Outline each blood parasite and name the species.
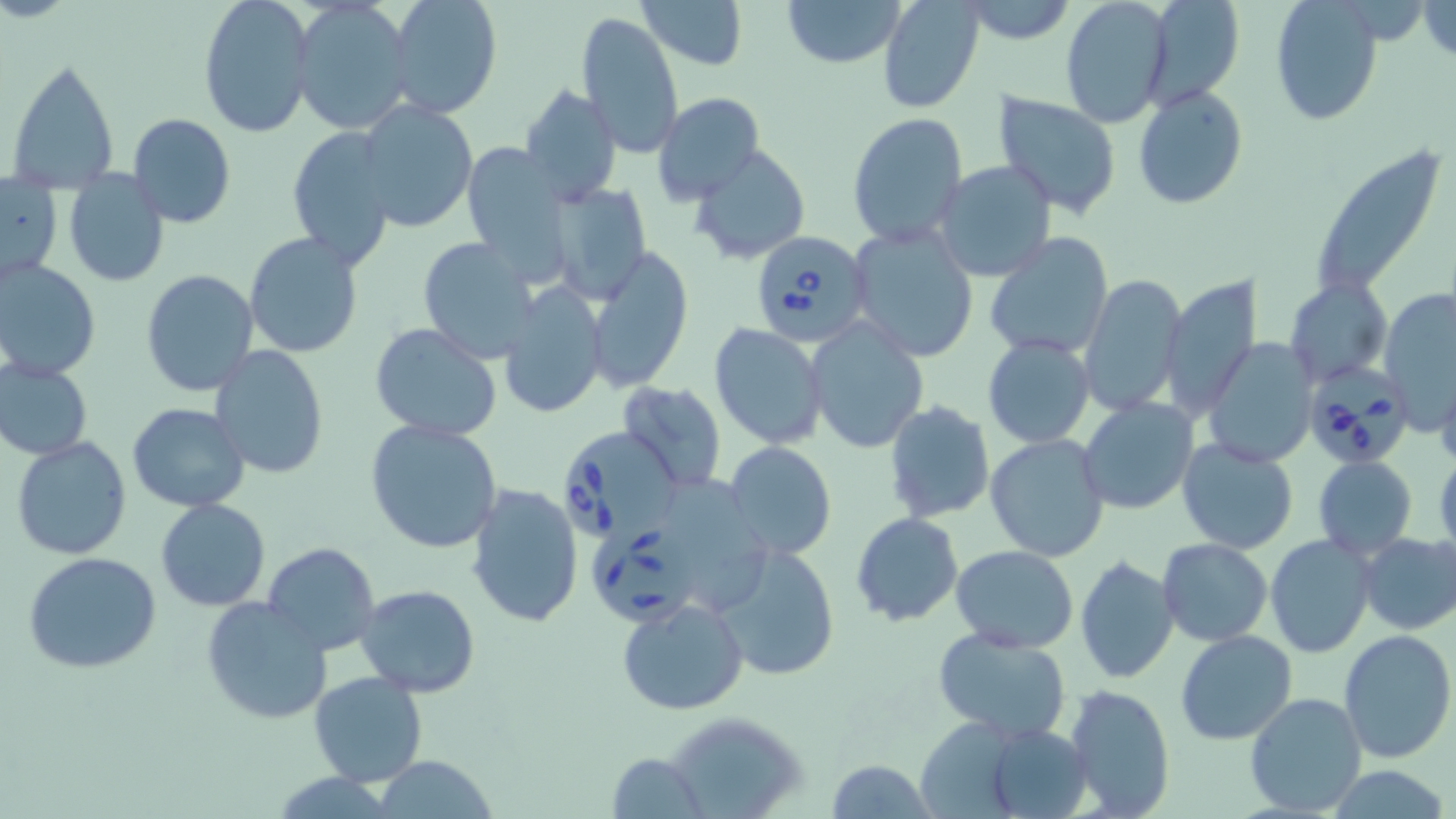
Approximate bounding boxes as [x1, y1, x2, y2] in pixels.
Babesia divergens-infected red blood cells: [749, 231, 874, 347], [1307, 359, 1413, 469], [560, 426, 683, 540], [586, 514, 697, 630].
No Plasmodium falciparum, Plasmodium ovale, Plasmodium malariae, Plasmodium vivax, or Trypanosoma brucei observed.

{
  "slide_level_diagnosis": "Babesia divergens",
  "uninfected_red_blood_cell_locations": "approximate bounding boxes as [x1, y1, x2, y2] in pixels: [198, 0, 316, 140], [386, 0, 501, 119], [636, 0, 747, 70], [781, 0, 906, 69], [876, 0, 985, 114], [1060, 0, 1174, 127], [1138, 0, 1243, 108], [291, 2, 415, 135], [1269, 2, 1382, 126], [578, 11, 682, 159], [7, 56, 121, 191], [518, 83, 623, 203], [1133, 85, 1248, 210], [992, 90, 1121, 220], [652, 93, 766, 207], [357, 99, 481, 232], [846, 111, 968, 250], [128, 112, 236, 228], [287, 126, 398, 268], [460, 140, 575, 278], [690, 144, 811, 266], [1320, 152, 1444, 294], [932, 160, 1058, 283], [62, 170, 170, 290], [1, 178, 63, 280], [545, 179, 652, 303], [846, 224, 979, 362], [244, 231, 364, 358], [984, 235, 1114, 360], [415, 236, 540, 364], [583, 245, 694, 393], [0, 257, 101, 382], [140, 271, 259, 396], [1079, 273, 1188, 417], [1160, 277, 1259, 419], [1285, 279, 1390, 387], [498, 281, 609, 420], [1378, 289, 1453, 427], [806, 316, 929, 454], [370, 323, 504, 442], [709, 323, 828, 450], [982, 336, 1096, 449], [1203, 337, 1320, 468], [210, 344, 329, 479], [0, 361, 93, 460], [1435, 371, 1456, 474], [614, 381, 726, 494], [1079, 397, 1199, 514], [882, 400, 994, 524], [127, 401, 249, 512], [365, 419, 504, 555], [986, 434, 1111, 561], [10, 436, 133, 560], [1175, 437, 1300, 554], [724, 441, 838, 558], [1433, 448, 1456, 557], [1314, 455, 1417, 561], [682, 480, 775, 602], [466, 484, 585, 628], [155, 498, 270, 611], [850, 511, 963, 627], [1355, 531, 1456, 635], [1265, 533, 1378, 659], [711, 538, 842, 681], [1156, 538, 1271, 645], [262, 541, 380, 655], [951, 545, 1078, 652], [25, 553, 162, 673], [1074, 554, 1180, 685], [356, 583, 483, 699], [201, 596, 332, 725], [616, 597, 749, 715], [931, 628, 1070, 742], [1174, 630, 1297, 745], [1338, 630, 1455, 763], [310, 672, 427, 787], [1061, 682, 1175, 818], [1243, 692, 1367, 819], [660, 710, 811, 819], [977, 720, 1095, 819], [607, 751, 708, 819], [372, 755, 499, 819], [825, 759, 937, 817], [1321, 765, 1451, 819]",
  "magnification": "1000x",
  "field_of_view": "one of a larger specimen",
  "modality": "optical microscopy",
  "image_size": "1456×819 pixels",
  "stain": "May-Grünwald-Giemsa",
  "preparation": "thin blood smear"
}